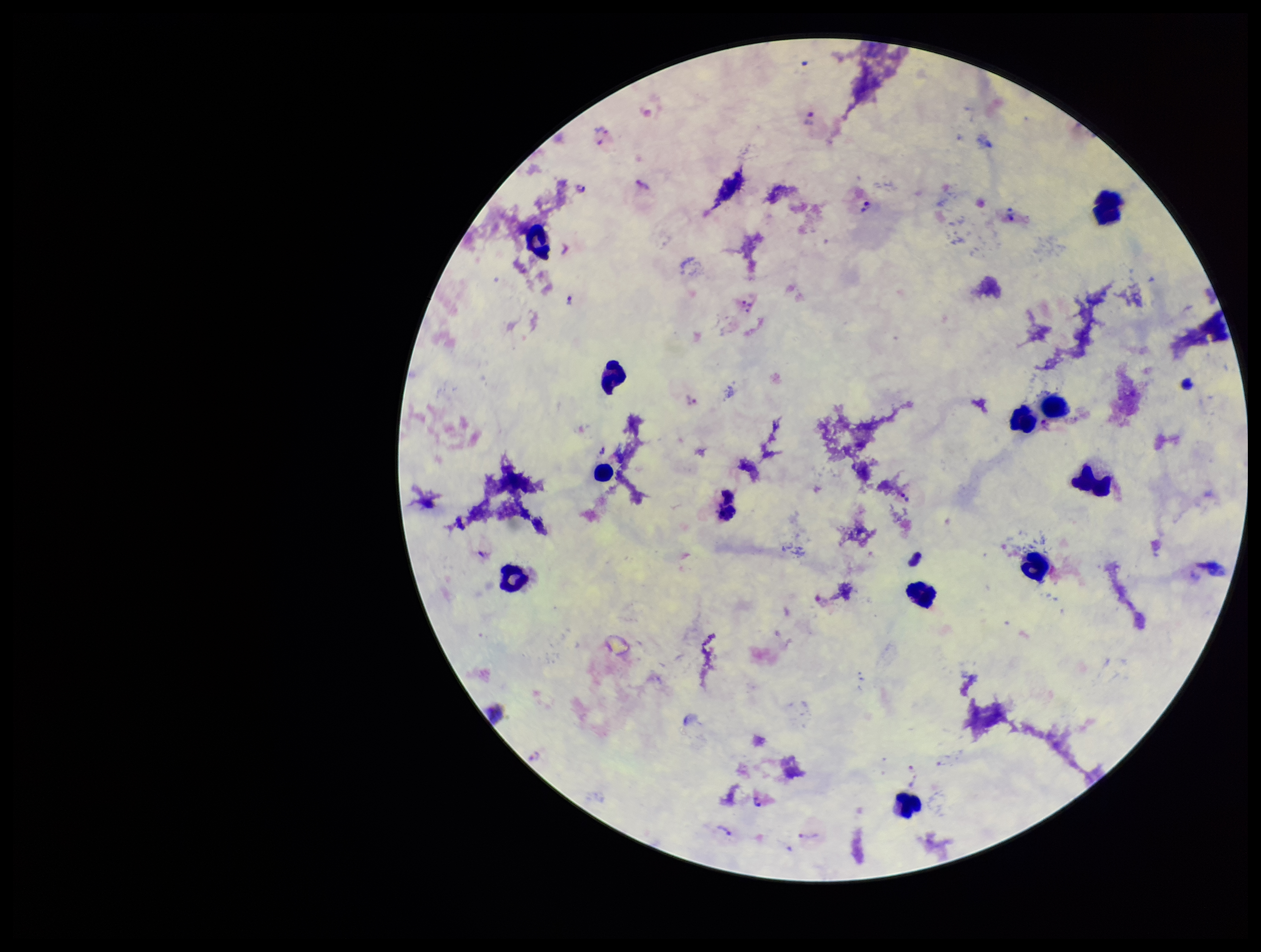
patient malaria status = infected
species reported for this patient = Plasmodium vivax
leukocyte count = 12
capture = smartphone photograph through the microscope eyepiece
field of view = one from this slide
image size = 1261×952 pixels
preparation = thick blood smear
stain = Giemsa
parasite count = 7
Plasmodium parasites = detected